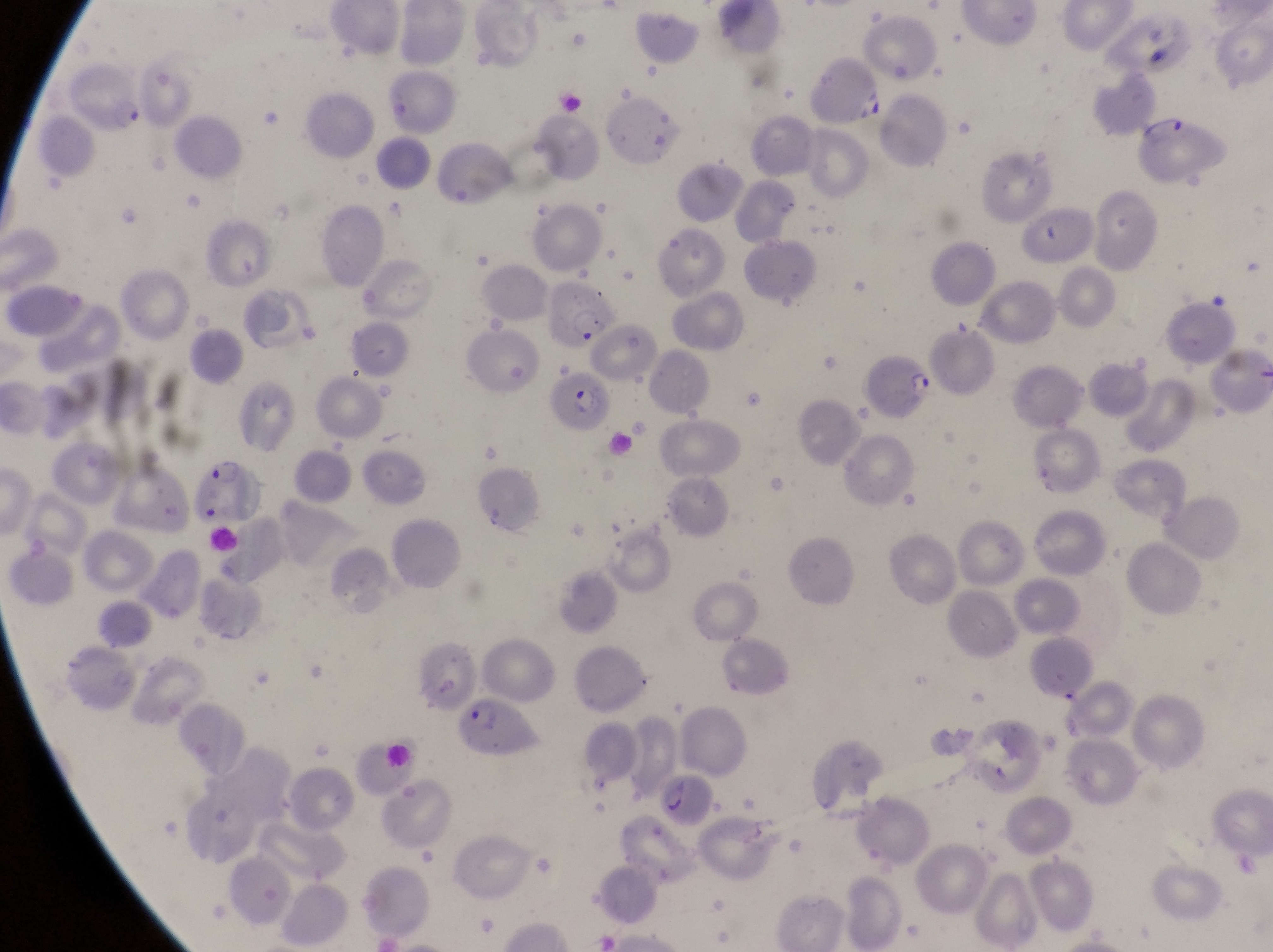

preparation = thin blood smear
parasitised red blood cell locations = approximate bounding boxes as [left, top, right, bottom] in pixels: [62, 57, 150, 147], [1141, 110, 1231, 192], [541, 277, 623, 351], [863, 348, 938, 420], [552, 360, 619, 434], [192, 447, 267, 532], [460, 691, 542, 763], [654, 771, 712, 829]
capture = smartphone photograph through the eyepiece of an Olympus CX-23 microscope
magnification = 1000x
field of view = single
image size = 1273×952 pixels
country = Uganda